Identify the blood parasite species.
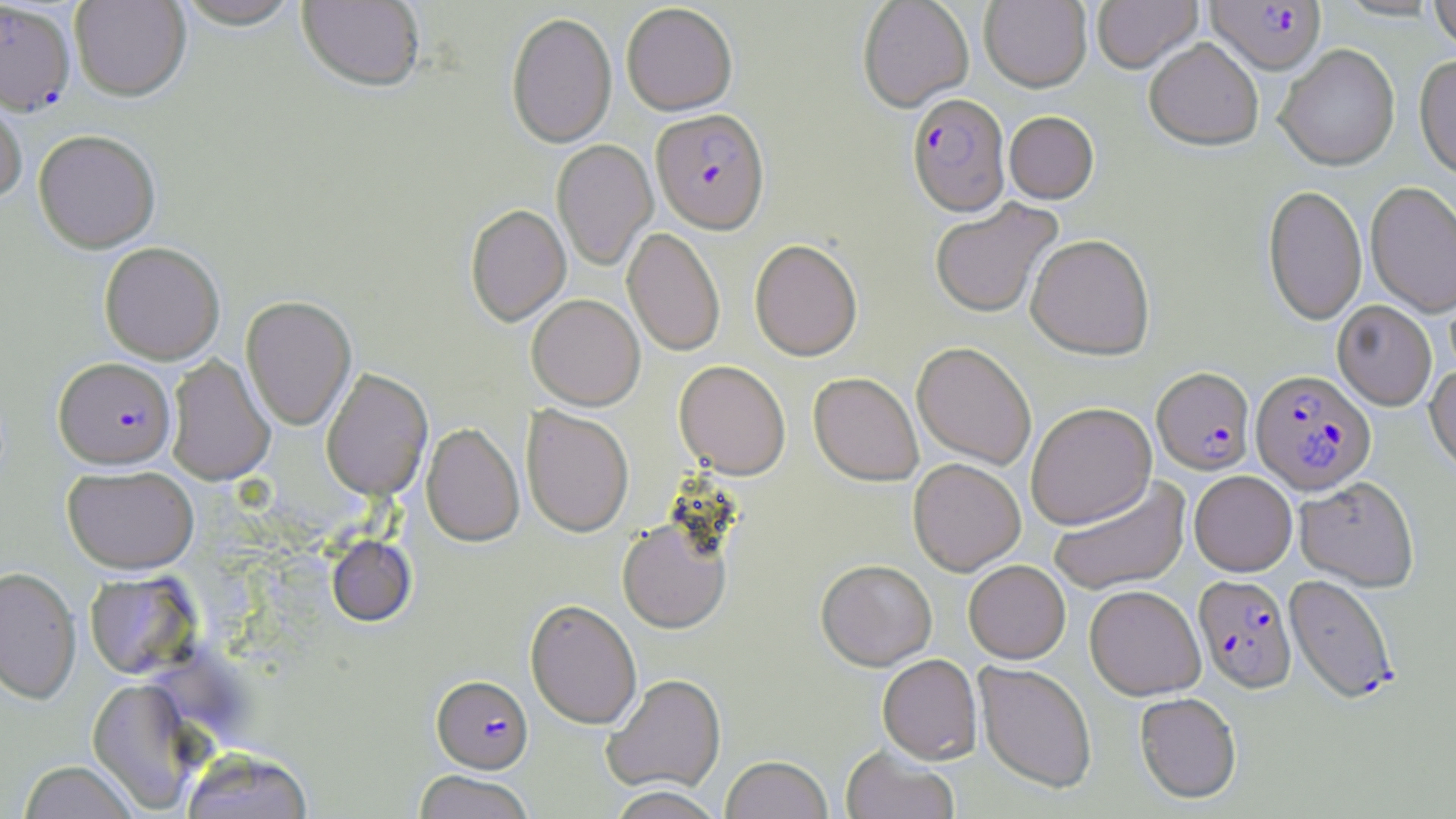
Plasmodium falciparum.

uninfected red blood cell locations = approximate bounding boxes as named x1/y1/x2/y2 corners in pixels: (x1=70, y1=0, x2=191, y2=101), (x1=175, y1=0, x2=302, y2=32), (x1=297, y1=0, x2=425, y2=94), (x1=857, y1=0, x2=974, y2=113), (x1=980, y1=0, x2=1092, y2=93), (x1=1092, y1=0, x2=1202, y2=75), (x1=1429, y1=0, x2=1456, y2=54), (x1=621, y1=3, x2=738, y2=116), (x1=506, y1=12, x2=617, y2=149), (x1=1144, y1=40, x2=1263, y2=153), (x1=1276, y1=45, x2=1400, y2=171), (x1=1414, y1=55, x2=1456, y2=183), (x1=0, y1=88, x2=27, y2=204), (x1=1004, y1=112, x2=1099, y2=204), (x1=34, y1=130, x2=160, y2=253), (x1=552, y1=139, x2=658, y2=271), (x1=1365, y1=182, x2=1456, y2=319), (x1=1263, y1=185, x2=1367, y2=326), (x1=930, y1=199, x2=1062, y2=319), (x1=465, y1=205, x2=571, y2=326), (x1=623, y1=228, x2=725, y2=357), (x1=1026, y1=235, x2=1154, y2=360), (x1=749, y1=240, x2=862, y2=361), (x1=99, y1=242, x2=225, y2=364), (x1=527, y1=294, x2=645, y2=410), (x1=241, y1=295, x2=356, y2=431), (x1=1333, y1=301, x2=1436, y2=411), (x1=911, y1=342, x2=1036, y2=470), (x1=165, y1=355, x2=275, y2=486), (x1=674, y1=360, x2=790, y2=479), (x1=1425, y1=364, x2=1456, y2=479), (x1=321, y1=369, x2=433, y2=501), (x1=808, y1=373, x2=923, y2=487), (x1=1026, y1=402, x2=1156, y2=530), (x1=521, y1=406, x2=634, y2=537), (x1=421, y1=424, x2=524, y2=547), (x1=908, y1=458, x2=1025, y2=575), (x1=62, y1=465, x2=198, y2=574), (x1=1189, y1=471, x2=1297, y2=576), (x1=1048, y1=477, x2=1190, y2=595), (x1=1295, y1=478, x2=1419, y2=591), (x1=618, y1=518, x2=732, y2=634), (x1=326, y1=535, x2=416, y2=627), (x1=816, y1=560, x2=937, y2=670), (x1=964, y1=560, x2=1070, y2=664), (x1=0, y1=566, x2=80, y2=703), (x1=85, y1=570, x2=200, y2=680), (x1=1084, y1=585, x2=1205, y2=700), (x1=525, y1=600, x2=641, y2=729), (x1=878, y1=654, x2=981, y2=764), (x1=974, y1=661, x2=1097, y2=793), (x1=602, y1=674, x2=726, y2=795), (x1=87, y1=678, x2=204, y2=813), (x1=1135, y1=692, x2=1242, y2=803), (x1=841, y1=745, x2=959, y2=819), (x1=180, y1=747, x2=314, y2=819), (x1=720, y1=756, x2=833, y2=819), (x1=18, y1=760, x2=140, y2=818), (x1=414, y1=770, x2=534, y2=819), (x1=604, y1=787, x2=727, y2=819)
field of view = one of a larger specimen
stain = May-Grünwald-Giemsa
image size = 1456×819 pixels
magnification = 1000x
modality = optical microscopy
Plasmodium falciparum-infected red blood cell locations = approximate bounding boxes as named x1/y1/x2/y2 corners in pixels: (x1=0, y1=1, x2=76, y2=115), (x1=1205, y1=1, x2=1326, y2=76), (x1=907, y1=94, x2=1010, y2=218), (x1=651, y1=110, x2=769, y2=235), (x1=54, y1=357, x2=176, y2=469), (x1=1152, y1=368, x2=1255, y2=476), (x1=1250, y1=370, x2=1377, y2=495), (x1=1194, y1=575, x2=1297, y2=692), (x1=1284, y1=575, x2=1399, y2=704), (x1=432, y1=675, x2=533, y2=774)
preparation = thin blood film